Describe the morphology of the erythrocytes.
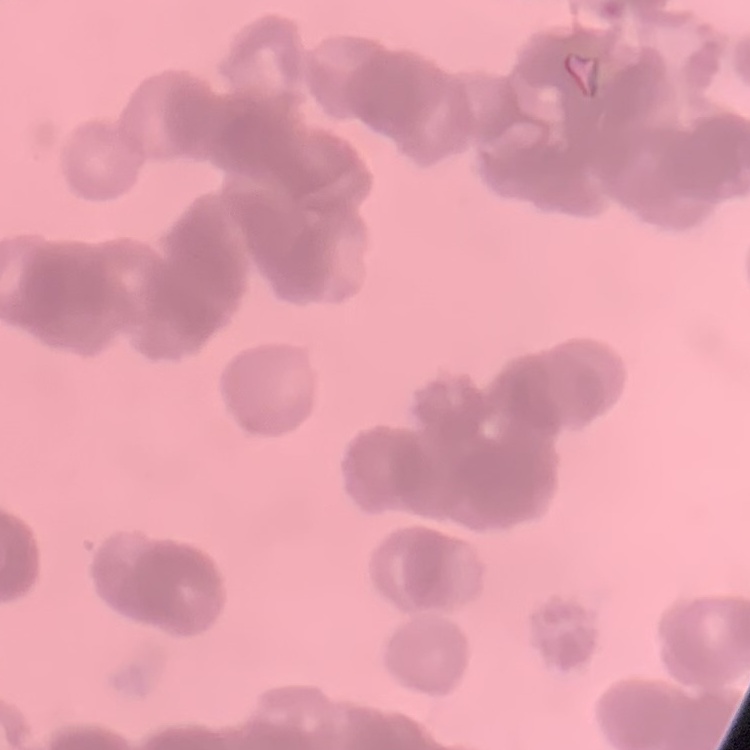

They show rouleaux formation.

Summary:
  - Image type: square crop of a larger photomicrograph
  - Stain: Field's or Giemsa
  - Preparation: thin peripheral smear